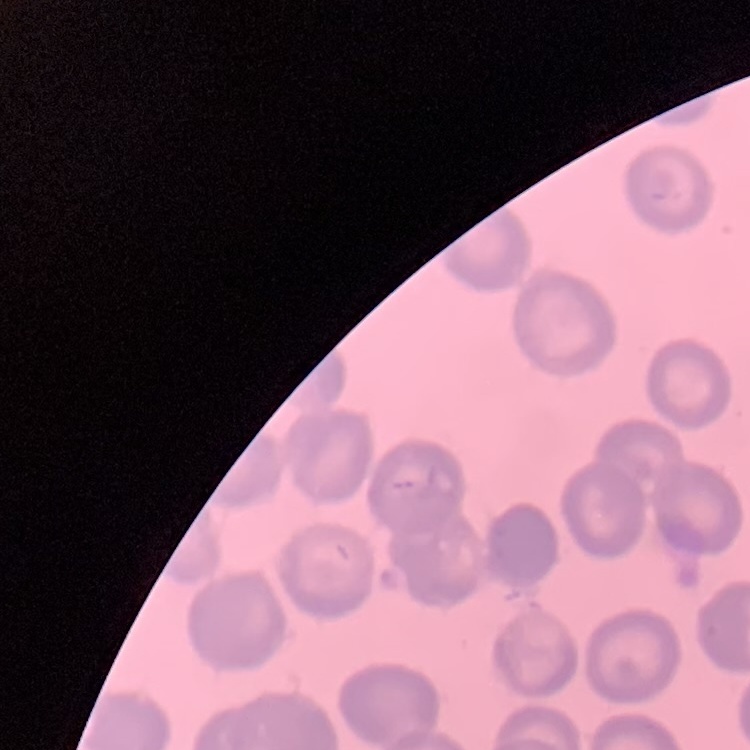
Summary:
  - Red blood cell morphology: no rouleaux formation
  - Image type: one tile cut from a larger photomicrograph
  - Stain: Field's or Giemsa
  - Preparation: thin blood smear